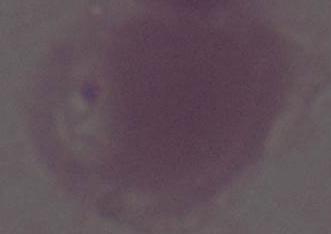 Captured at 1000x magnification. A red blood cell is shown. Micrograph.